Report the malaria status of this cell.
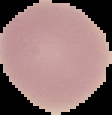

Uninfected.

Summary:
  - Image size: 112×115 pixels
  - Image type: segmented cell region on a black background
  - Preparation: thin blood smear